Assess the morphology of the red blood cells.
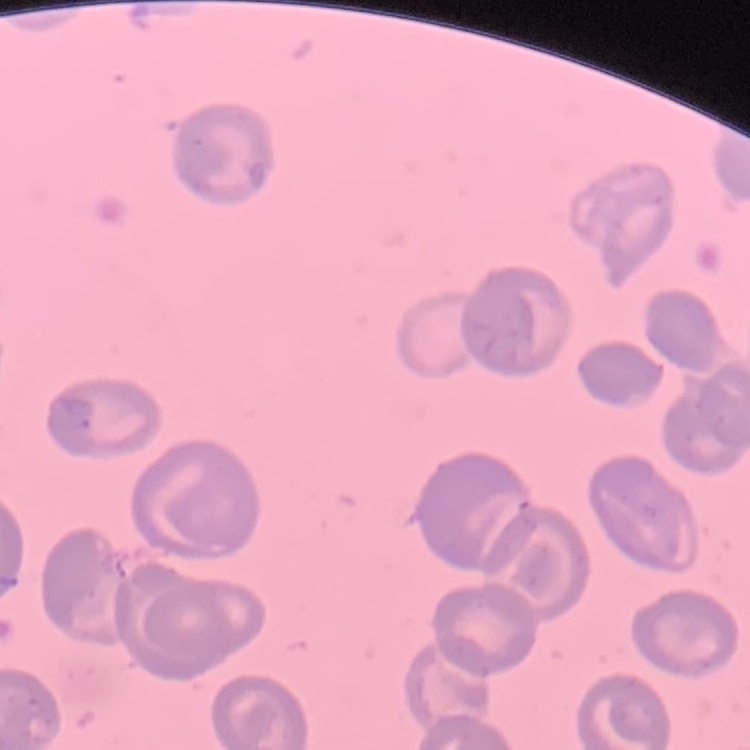
No rouleaux formation.

Summary:
  - Stain: Field's or Giemsa
  - Image type: square crop of a larger photomicrograph
  - Preparation: thin blood film